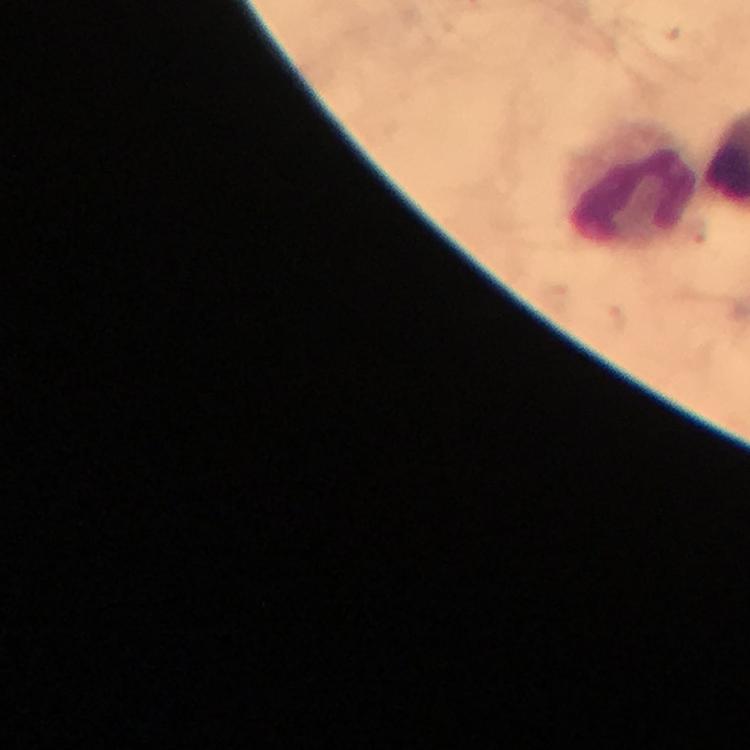
magnification = 100x
stain = Giemsa
immersion oil = applied
preparation = thick blood smear
image size = 750×750 pixels
context = from a malaria diagnostic workup
Plasmodium parasites = none detected
capture = smartphone mounted on the microscope
leukocyte locations = approximate centers as {x, y} in pixels: {631, 188}
cropped from = a single field of view